State which parasite is depicted.
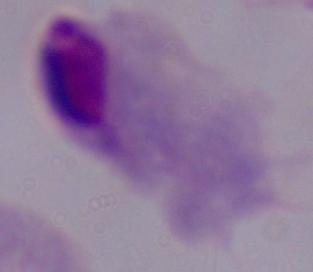
This is a trichomonad.

{
  "modality": "micrograph",
  "magnification": "1000x"
}